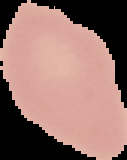

image type = cell region segmented out of the field of view; surrounding area masked to black
preparation = thin blood film
result = negative for malaria parasites
image size = 127×160 pixels